Give the extent of all Plasmodium parasites.
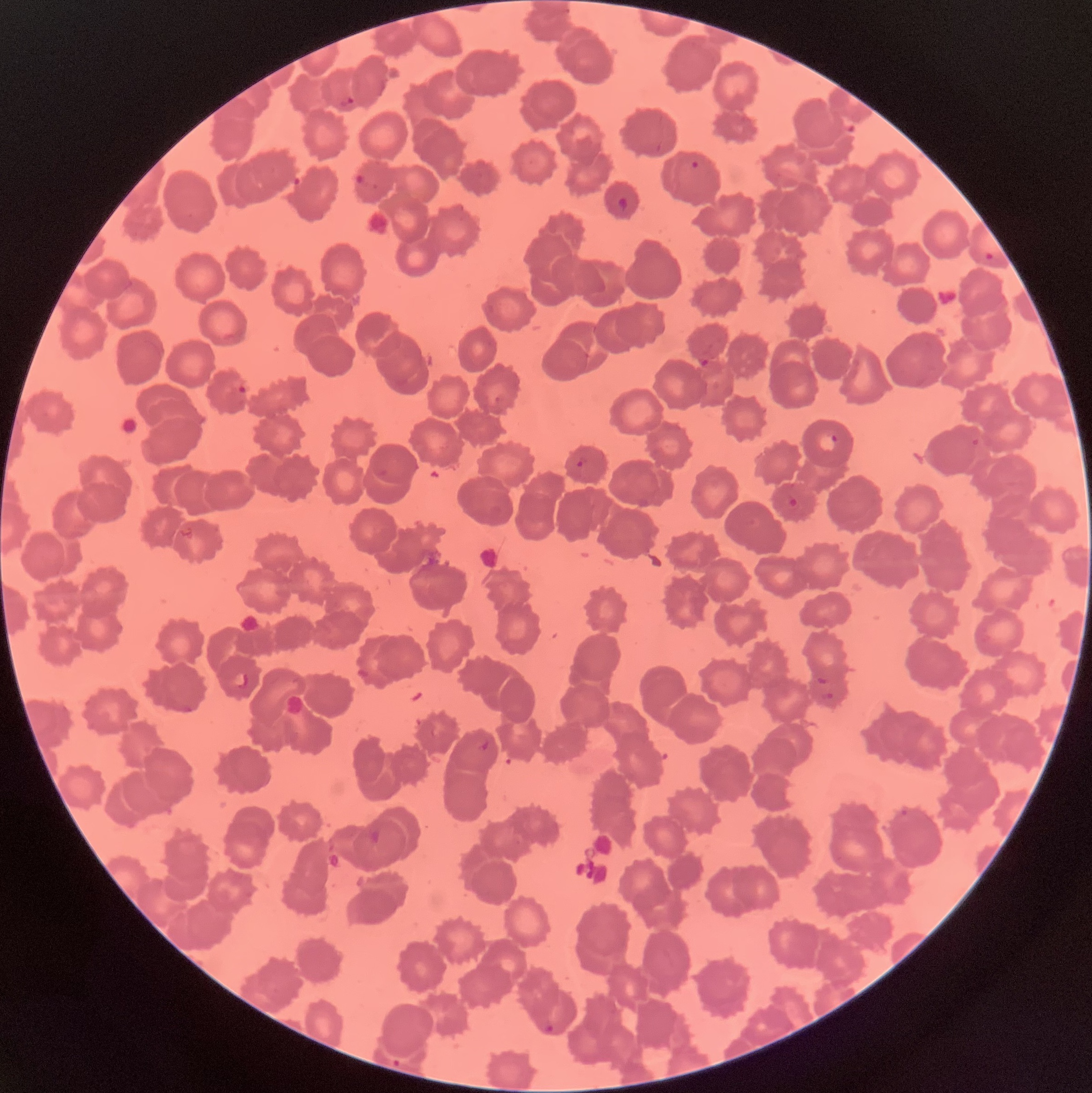
Approximate bounding boxes as (x1,y1)-(x2,y2) corner pairs in pixels.
Plasmodium parasites: (339,95)-(356,107), (841,114)-(860,134), (690,159)-(701,171), (353,170)-(365,187), (617,196)-(630,210), (984,250)-(995,261), (237,382)-(248,396), (818,431)-(839,453), (576,454)-(588,468), (787,493)-(799,510), (233,670)-(249,690), (815,675)-(829,685), (821,690)-(835,703), (478,738)-(492,755), (543,1021)-(556,1034), (392,1057)-(403,1069).

Light microscopy. The red blood cells show rouleaux formation. Thin blood film. Image is 1092×1093 pixels.